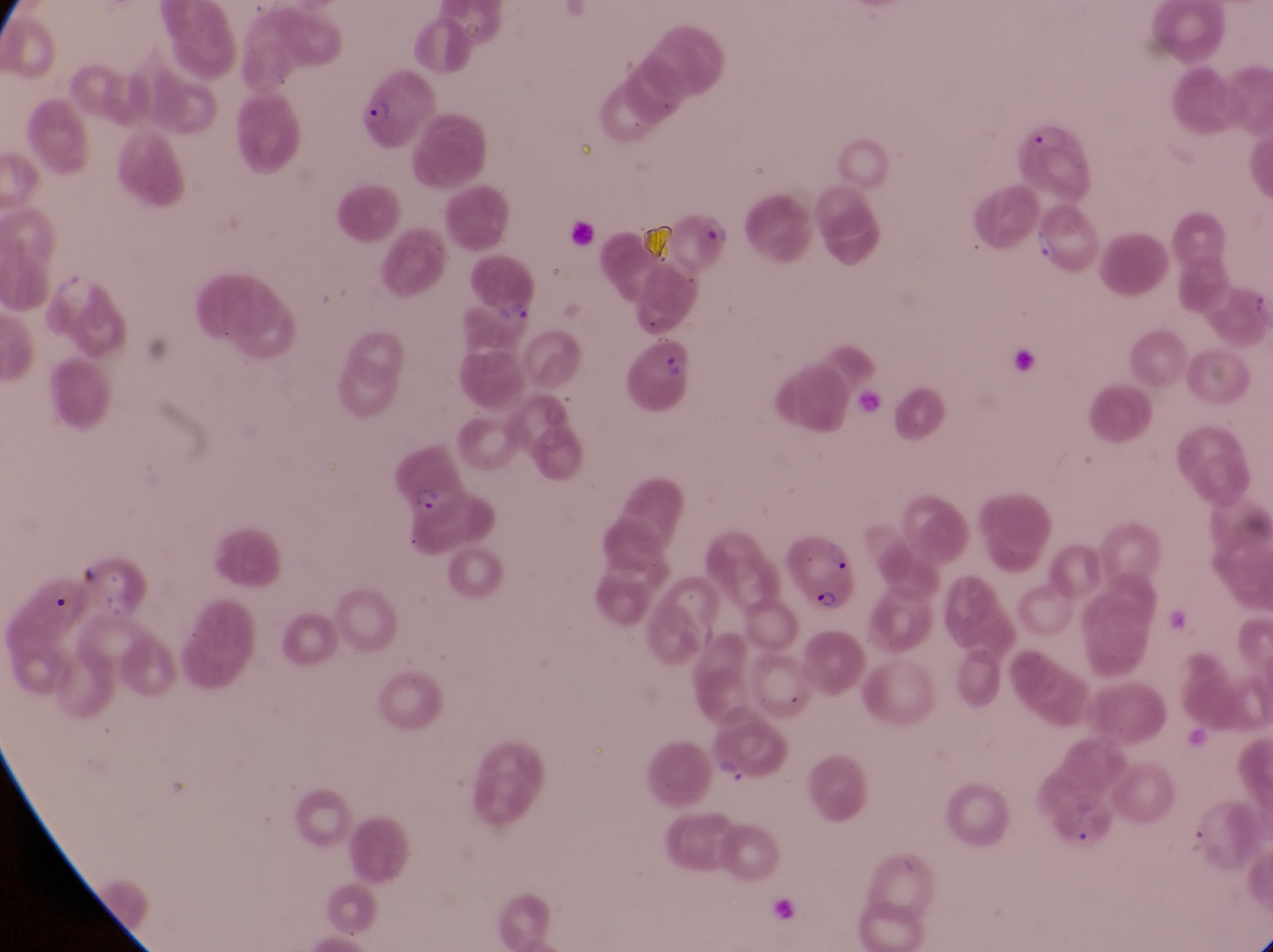

image_size: 1273×952 pixels
capture: smartphone photograph through the eyepiece of an Olympus CX-23 microscope
country: Uganda
magnification: 1000x
trophozoite_locations: 'approximate bounding boxes as (left, top, right, bottom) in pixels: (1025, 220, 1060, 268), (714, 754, 764, 797)'
parasitised_red_blood_cell_locations: 'approximate bounding boxes as (left, top, right, bottom) in pixels: (350, 74, 430, 149), (1011, 118, 1094, 198), (470, 259, 540, 321), (637, 337, 694, 402), (389, 442, 477, 527), (782, 534, 864, 612)'
artifact_platelet_like_body_stain_precipitate_or_debris_locations: 'approximate bounding boxes as (left, top, right, bottom) in pixels: (565, 218, 590, 240), (636, 218, 676, 258)'
preparation: thin blood film
field_of_view: single